Assess this cell for malaria.
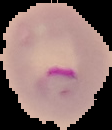

It is parasitized.

image type = cell region segmented out of the field of view; surrounding area masked to black
image size = 112×130 pixels
preparation = thin blood film